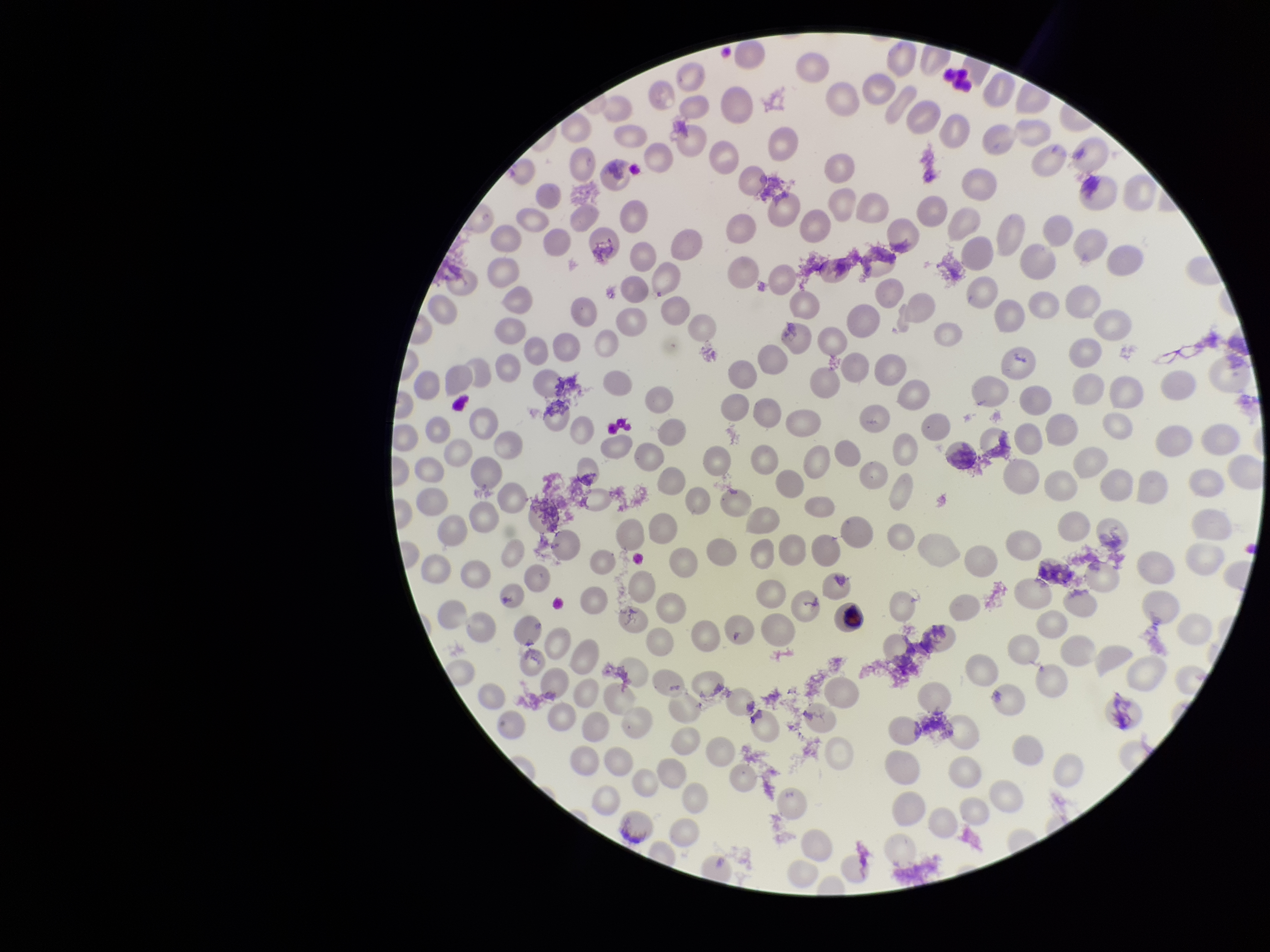

Summary:
  - Field of view: one from this slide
  - Stain: Giemsa
  - Parasitized red blood cells: none detected
  - Parasitized red blood cell count: 0
  - Preparation: thin smear
  - Capture: smartphone photograph through the microscope eyepiece
  - Image size: 1270×952 pixels
  - Patient malaria status: negative
  - Red blood cell count: 231